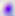
magnification = 400x
identification = Toxoplasma gondii
modality = micrograph